State the blood parasite species.
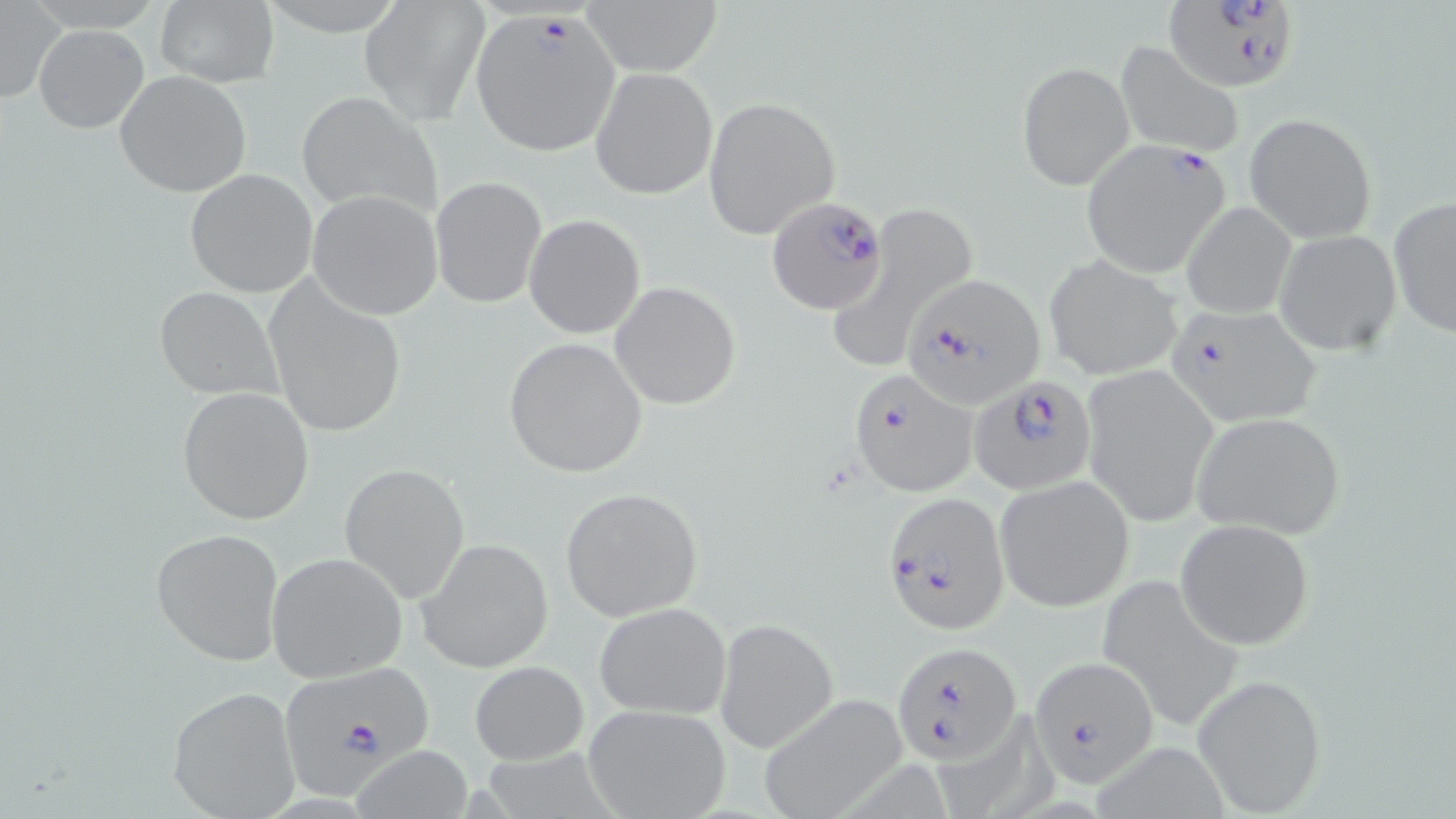
Plasmodium falciparum.

modality = optical microscopy
Plasmodium falciparum-infected red blood cell locations = approximate bounding boxes as (x1,y1)-(x2,y2) corner pairs in pixels: (1166,1)-(1294,86), (471,9)-(622,156), (1082,141)-(1230,277), (768,197)-(890,315), (901,275)-(1045,408), (1162,301)-(1323,427), (848,368)-(979,498), (970,374)-(1095,496), (887,499)-(1012,635), (891,640)-(1021,764), (1029,655)-(1159,789), (275,659)-(436,789)
uninfected red blood cell locations = approximate bounding boxes as (x1,y1)-(x2,y2) corner pairs in pixels: (154,0)-(278,88), (360,0)-(490,122), (580,0)-(723,77), (0,3)-(64,104), (33,25)-(149,134), (1115,42)-(1246,158), (1018,61)-(1135,190), (589,67)-(718,200), (114,70)-(252,197), (295,92)-(440,217), (702,96)-(841,239), (1245,113)-(1377,242), (185,169)-(319,299), (431,177)-(546,308), (306,190)-(444,320), (1389,196)-(1455,340), (1182,200)-(1296,318), (831,201)-(977,372), (524,214)-(646,340), (1274,231)-(1401,355), (1046,255)-(1183,382), (264,277)-(410,440), (611,281)-(742,410), (153,286)-(283,401), (503,336)-(649,478), (1081,363)-(1219,526), (175,387)-(315,524), (1189,410)-(1346,538), (339,462)-(472,602), (995,475)-(1134,612), (559,487)-(704,621), (1176,518)-(1316,649), (150,527)-(284,668), (416,538)-(554,672), (266,552)-(407,682), (1094,571)-(1244,729), (593,602)-(734,718), (714,618)-(837,752), (470,660)-(590,765), (1192,673)-(1328,815), (166,685)-(302,818), (755,694)-(910,818), (581,703)-(731,819), (1093,737)-(1235,818), (354,744)-(474,817)
magnification = 1000x
stain = May-Grünwald-Giemsa
image size = 1456×819 pixels
preparation = thin blood film
field of view = one of a larger specimen